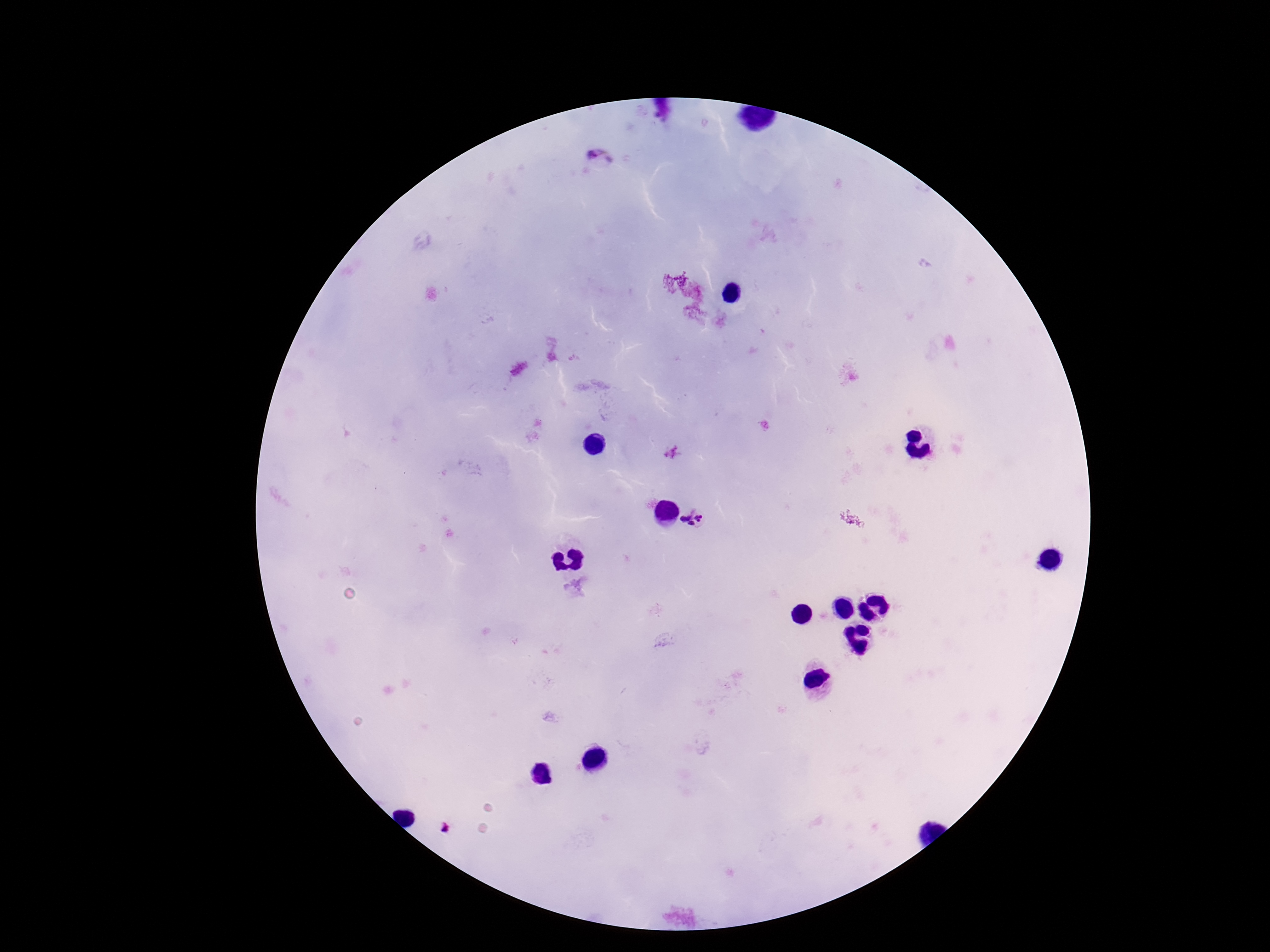

plasmodium_parasite_locations: 'approximate centers as {x, y} in pixels: {601, 161}, {694, 518}, {448, 831}'
image_size: 1270×952 pixels
field_of_view: single
preparation: thick peripheral-blood smear
patient_malaria_status: infected
magnification: 100x
stain: Giemsa
capture: smartphone camera through the microscope eyepiece